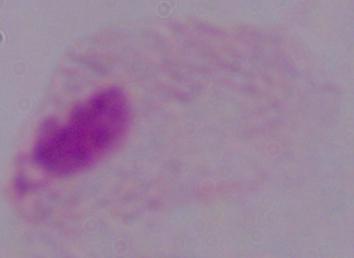

{
  "identification": "trichomonad",
  "modality": "photomicrograph",
  "magnification": "1000x"
}